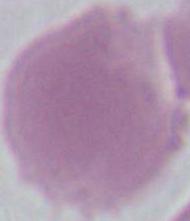

A red blood cell is shown. 1000x magnification. Micrograph.